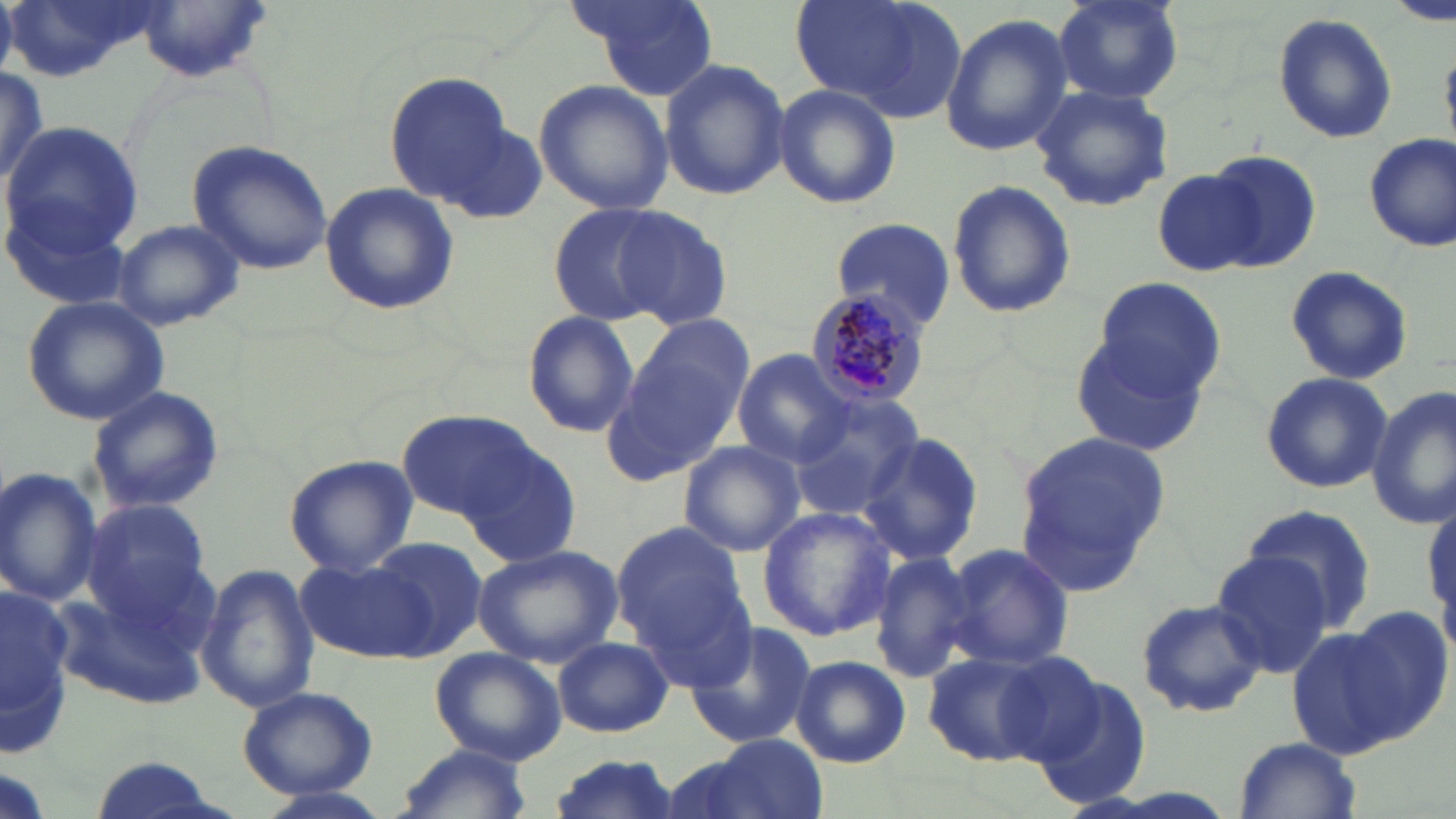

slide-level diagnosis = Plasmodium malariae
field of view = one of a larger specimen
preparation = thin blood film
magnification = 1000x
stain = May-Grünwald-Giemsa
uninfected red blood cell locations = approximate bounding boxes as (x1,y1)-(x2,y2) corner pairs in pixels: (0,0)-(163,83), (573,0)-(716,100), (794,0)-(967,122), (1056,0)-(1183,105), (1392,0)-(1455,25), (0,3)-(16,79), (1272,11)-(1400,146), (940,14)-(1073,158), (658,57)-(789,200), (0,63)-(55,191), (383,70)-(520,208), (534,78)-(673,214), (772,83)-(902,210), (1029,84)-(1175,212), (426,114)-(551,228), (1,120)-(144,255), (1363,134)-(1455,251), (188,139)-(336,275), (1199,150)-(1322,273), (1154,170)-(1262,276), (946,179)-(1077,320), (319,181)-(460,318), (5,198)-(134,311), (550,205)-(668,323), (609,206)-(733,331), (110,218)-(243,331), (828,218)-(956,333), (1283,265)-(1414,387), (1094,278)-(1228,398), (22,296)-(171,425), (519,311)-(641,438), (612,322)-(752,477), (1071,333)-(1212,456), (731,352)-(852,469), (1259,371)-(1393,494), (87,385)-(224,515), (1367,387)-(1456,529), (787,392)-(924,523), (397,409)-(533,521), (858,427)-(986,567), (1015,430)-(1172,581), (460,434)-(585,568), (678,440)-(806,558), (286,456)-(418,574), (0,468)-(102,609), (78,499)-(222,644), (1242,504)-(1380,635), (757,505)-(894,642), (612,519)-(751,672), (362,536)-(487,659), (943,541)-(1075,672), (472,543)-(624,669), (1211,548)-(1338,679), (870,550)-(980,685), (298,557)-(438,663), (197,564)-(320,712), (46,579)-(220,715), (0,587)-(86,754), (1135,597)-(1266,718), (1340,604)-(1454,741), (682,618)-(817,753), (1287,626)-(1402,757), (553,636)-(672,738), (430,647)-(566,765), (921,647)-(1077,767), (789,655)-(911,766), (1031,674)-(1155,809), (236,686)-(379,801), (698,734)-(828,819), (1233,737)-(1363,818), (393,744)-(534,819), (544,752)-(683,819), (90,754)-(226,819), (246,785)-(396,819)
modality = light microscopy
Plasmodium malariae-infected red blood cell locations = approximate bounding boxes as (x1,y1)-(x2,y2) corner pairs in pixels: (803,287)-(933,409)
image size = 1456×819 pixels